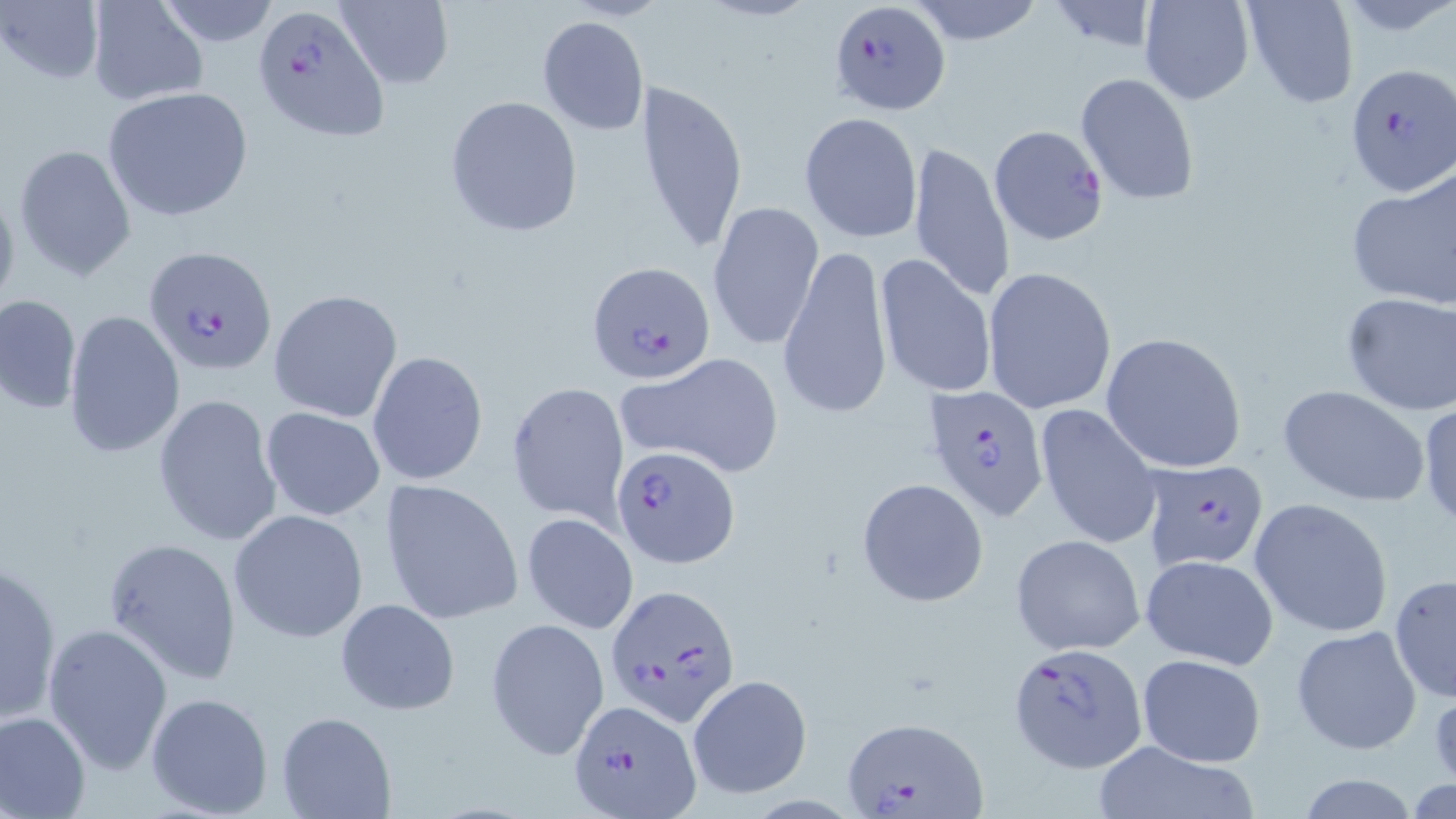
Approximate bounding boxes as [x1, y1, x2, y2] in pixels. Uninfected red blood cell locations: [154, 0, 280, 47], [334, 0, 453, 90], [907, 0, 1045, 45], [1139, 0, 1254, 104], [1240, 0, 1359, 109], [1, 1, 104, 88], [86, 1, 207, 106], [1043, 1, 1163, 54], [537, 16, 649, 135], [1078, 72, 1199, 203], [634, 76, 751, 257], [102, 86, 254, 222], [445, 95, 585, 237], [799, 114, 923, 245], [907, 139, 1015, 305], [14, 143, 137, 281], [1346, 167, 1456, 309], [0, 179, 21, 320], [707, 200, 823, 351], [777, 242, 890, 421], [877, 254, 999, 400], [982, 266, 1117, 415], [270, 287, 403, 421], [1340, 291, 1456, 416], [0, 293, 81, 414], [63, 311, 185, 458], [1100, 332, 1248, 473], [366, 350, 488, 487], [629, 354, 783, 478], [505, 380, 630, 526], [1277, 384, 1432, 507], [153, 394, 282, 550], [1417, 399, 1456, 531], [1036, 404, 1162, 550], [260, 407, 386, 522], [856, 478, 988, 607], [378, 479, 523, 625], [1249, 498, 1393, 638], [229, 509, 369, 644], [522, 513, 639, 636], [1011, 533, 1145, 656], [102, 536, 243, 685], [1140, 554, 1278, 671], [1, 556, 63, 726], [1389, 573, 1455, 703], [335, 598, 460, 715], [487, 617, 609, 760], [42, 625, 172, 773], [1289, 626, 1423, 754], [1136, 652, 1268, 767], [687, 673, 813, 799], [146, 690, 275, 817], [0, 709, 91, 819], [277, 710, 396, 818], [1085, 740, 1261, 819], [1293, 775, 1427, 817]. Plasmodium falciparum-infected red blood cell locations: [830, 0, 951, 117], [249, 5, 390, 141], [1345, 63, 1453, 195], [987, 123, 1109, 246], [144, 246, 277, 376], [587, 260, 716, 385], [924, 383, 1051, 524], [609, 445, 738, 569], [1139, 458, 1268, 571], [605, 583, 740, 726], [1009, 642, 1147, 771], [569, 700, 702, 816], [840, 713, 991, 819]. Slide-level diagnosis: Plasmodium falciparum. Thin blood film. Image is 1456×819 pixels. May-Grünwald-Giemsa stain. Optical microscopy. 1000x magnification. One field of a larger specimen.